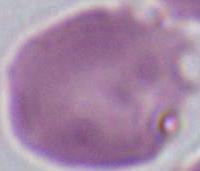

magnification = 1000x
identification = erythrocyte
modality = photomicrograph